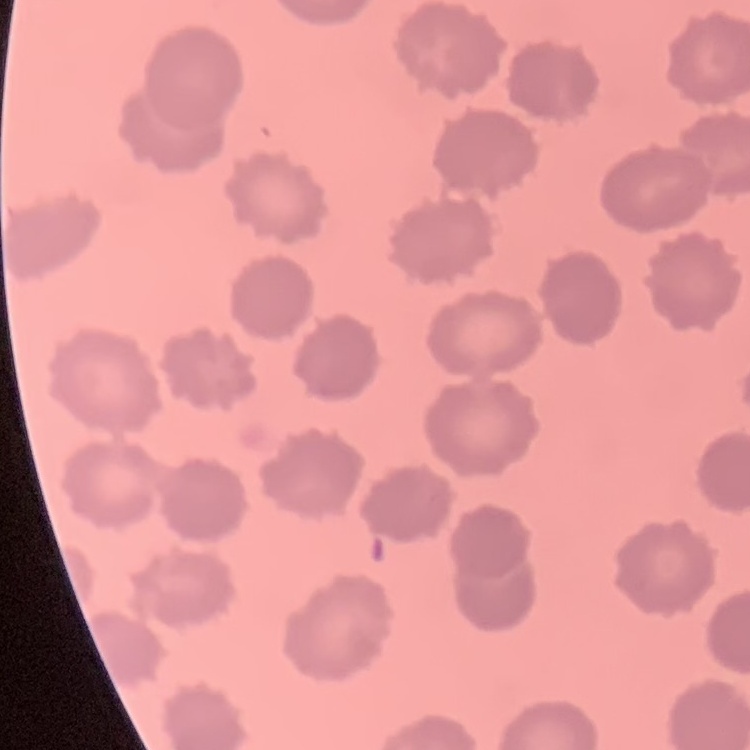
Summary:
  - Red blood cell morphology: no rouleaux formation
  - Stain: Field's or Giemsa
  - Preparation: thin peripheral smear
  - Image type: one tile cut from a larger photomicrograph